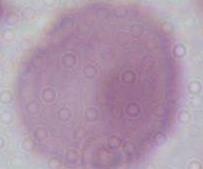

Summary:
  - Magnification: 1000x
  - Identification: erythrocyte
  - Modality: photomicrograph